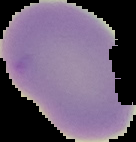

{
  "image_type": "cell region segmented out of the field of view; surrounding area masked to black",
  "image_size": "136×142 pixels",
  "result": "no malaria parasites seen",
  "preparation": "thin blood film"
}